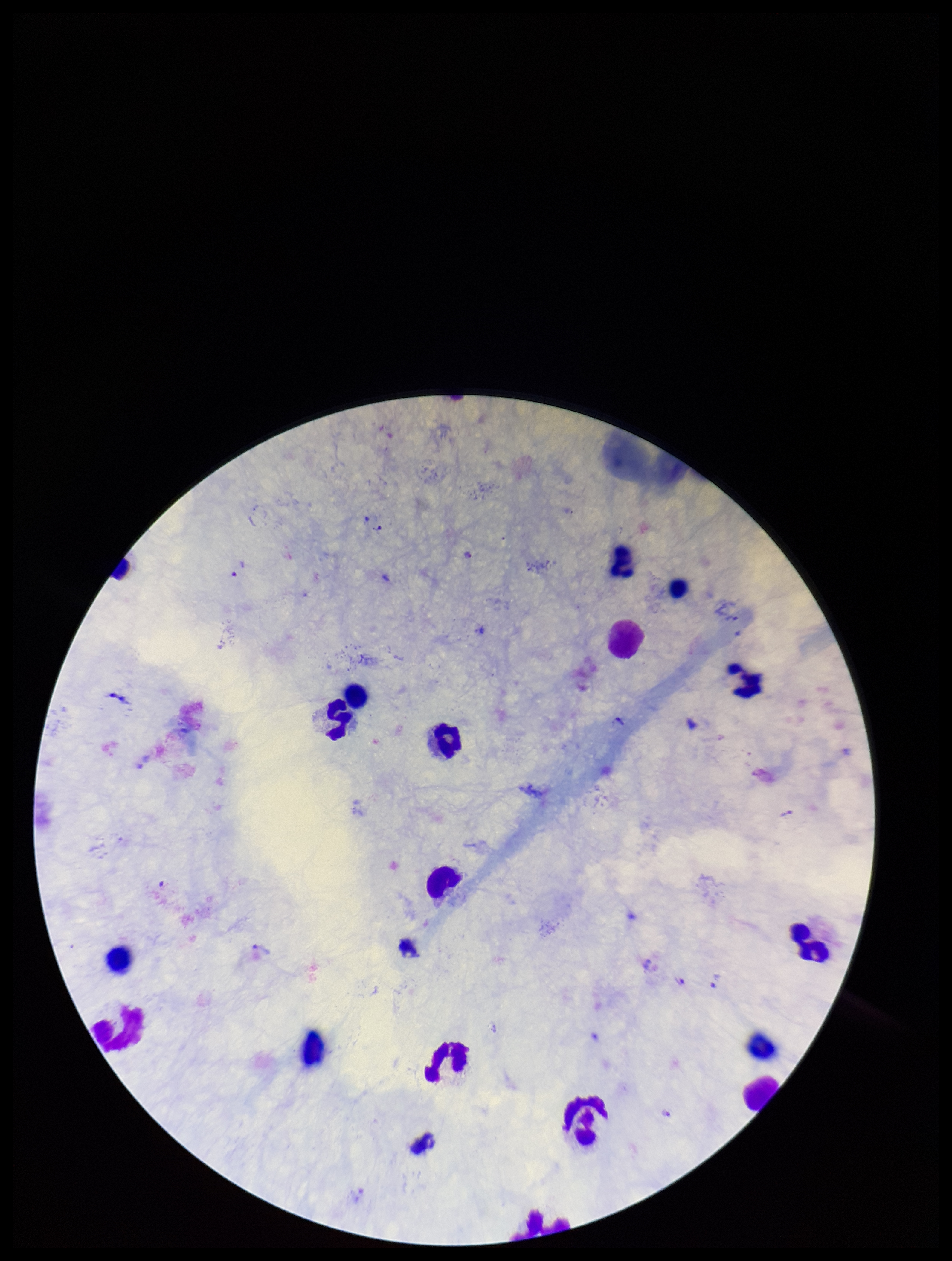 Plasmodium parasites: seen. Patient malaria status: positive. Parasite count: 4. Image is 952×1261 pixels. Leukocyte count: 17. Photographed through the microscope eyepiece with a smartphone camera. Species reported for this patient: Plasmodium vivax. Preparation: thick smear. Giemsa stain. One field from this slide.